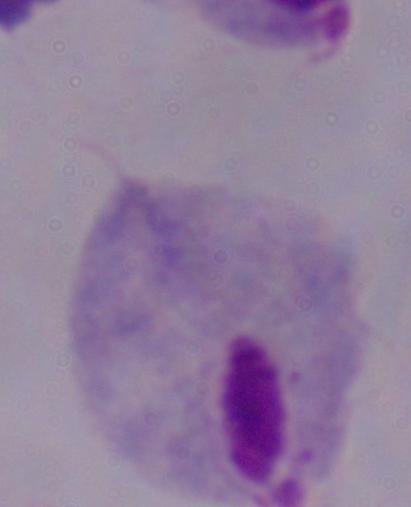

identification = trichomonad
modality = photomicrograph
magnification = 1000x